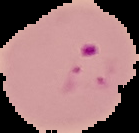 Cell region segmented out of the field of view; the surrounding area is masked to black. From a thin blood smear. Result: Plasmodium parasites detected. Image is 139×133 pixels.